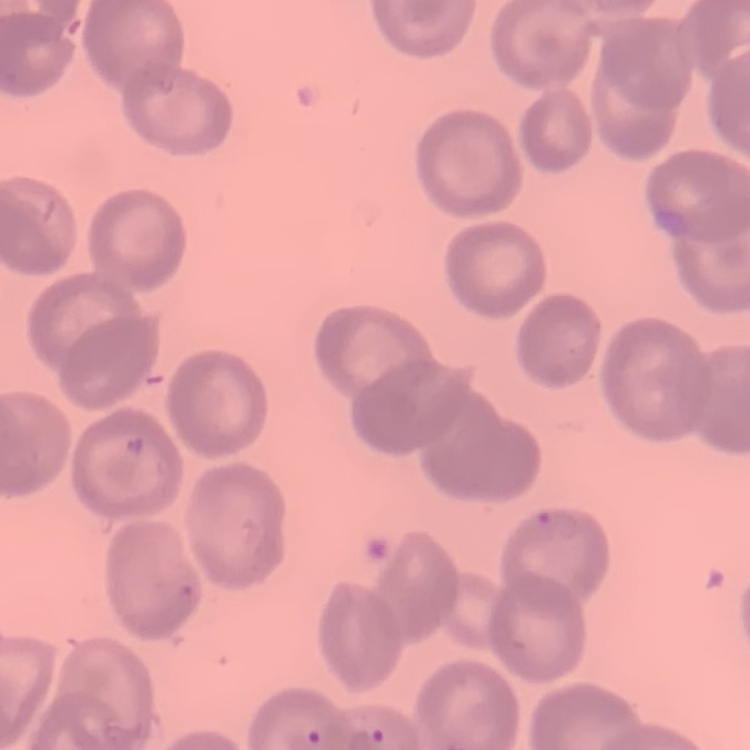
Summary:
  - Erythrocyte morphology: no rouleaux formation
  - Stain: Field's or Giemsa
  - Image type: square crop of a larger photomicrograph
  - Preparation: thin blood smear